Assess the morphology of the erythrocytes.
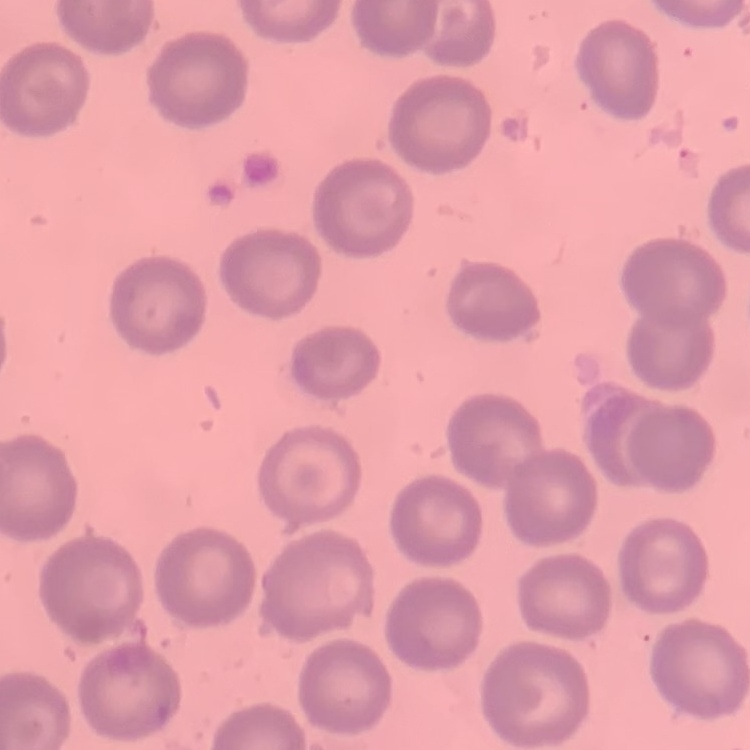
No rouleaux formation.

Field's or Giemsa stain. One tile cut from a larger photomicrograph. Thin peripheral smear.